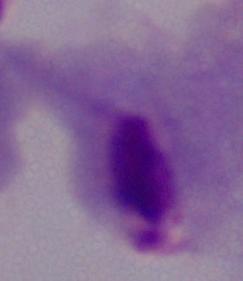
Summary:
  - Modality: photomicrograph
  - Magnification: 1000x
  - Identification: trichomonad